Name the parasite shown.
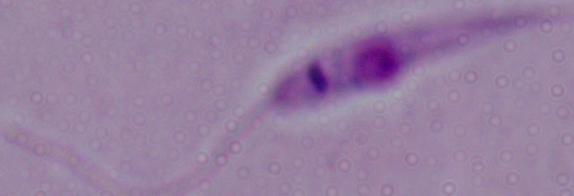
Leishmania.

Micrograph. 1000x magnification.